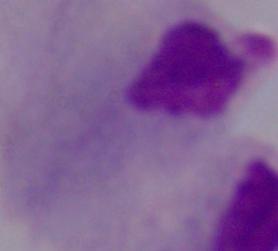
Summary:
  - Magnification: 1000x
  - Modality: photomicrograph
  - Identification: trichomonad